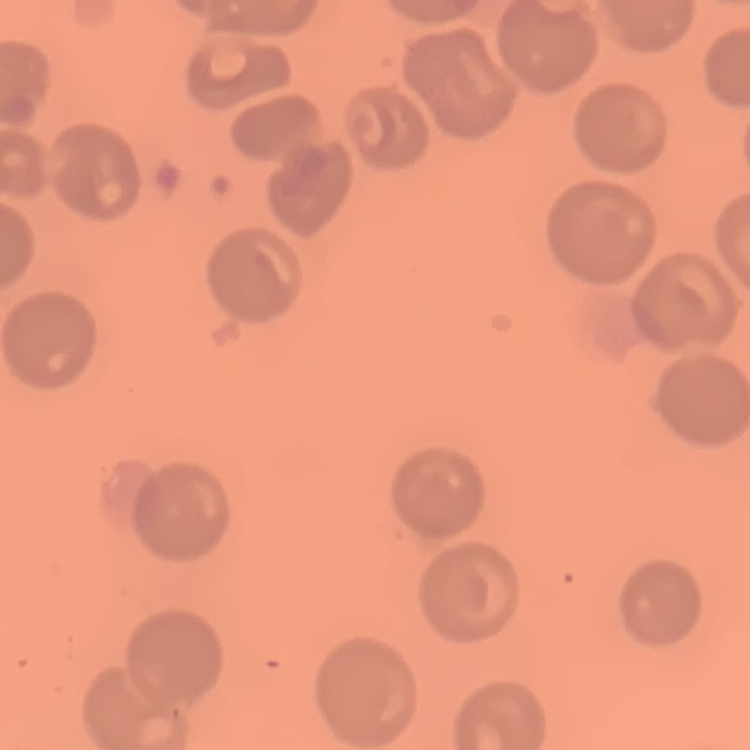
The erythrocytes show no rouleaux formation. Thin blood smear. Square crop of a larger photomicrograph. Stained with either Field's or Giemsa.